Report the malaria status of this cell.
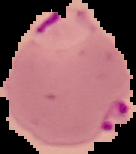

Parasitized.

Summary:
  - Preparation: thin blood film
  - Image type: cell region segmented out of the field of view; surrounding area masked to black
  - Image size: 136×154 pixels